Give the position of every Plasmodium parasite.
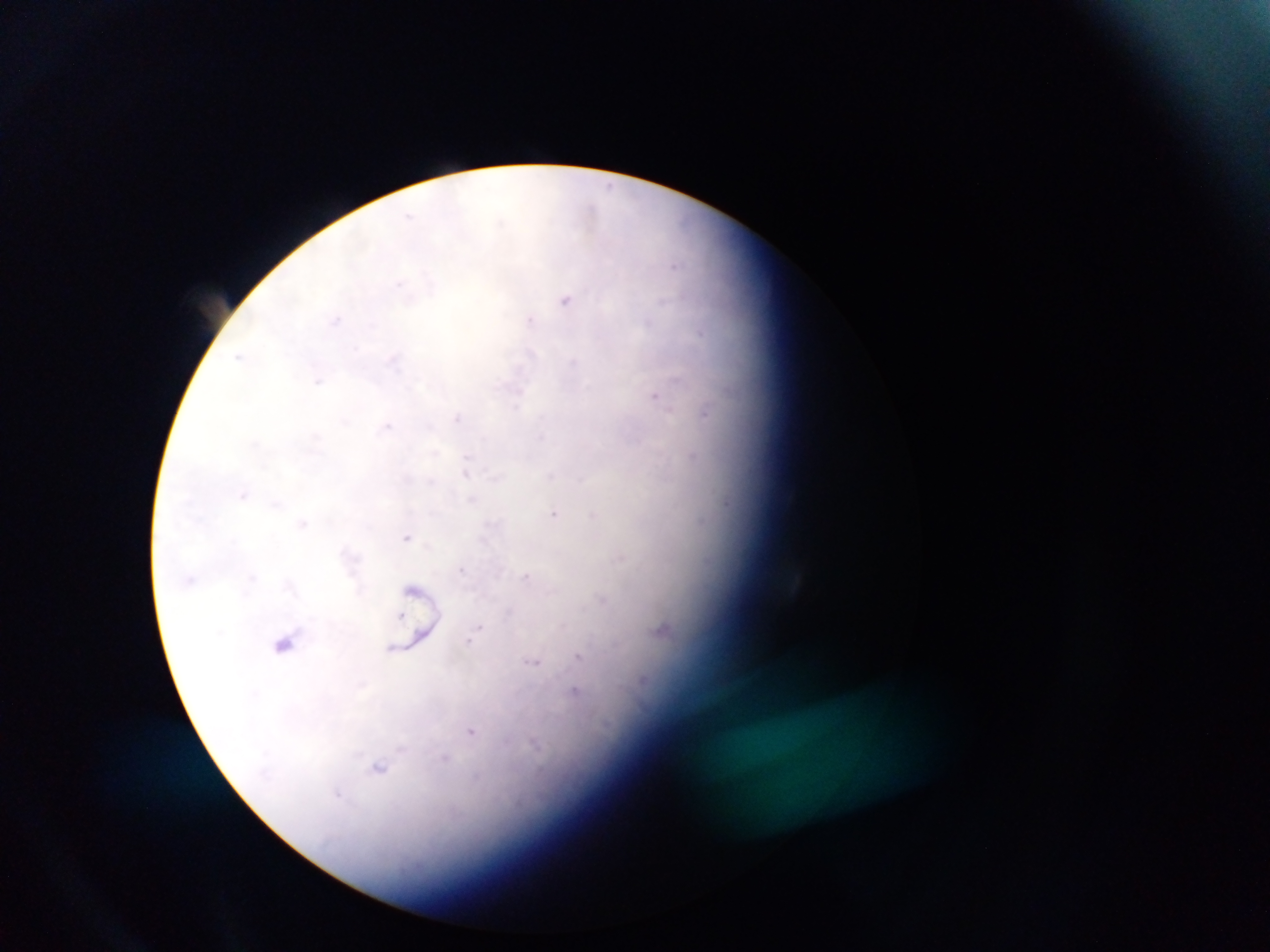
Approximate centers as {x, y} in pixels.
Plasmodium parasites: {592, 212}, {567, 299}, {530, 319}, {656, 395}, {705, 414}, {457, 417}, {388, 426}, {694, 455}, {466, 470}, {244, 494}, {726, 504}, {554, 513}, {594, 515}, {304, 523}, {407, 536}, {622, 558}, {463, 570}, {528, 576}, {602, 599}, {402, 616}, {479, 628}, {661, 630}, {471, 640}, {284, 644}, {579, 656}, {535, 662}, {577, 693}, {472, 731}, {379, 766}, {339, 794}.

Single field of view. Photographed through a microscope with a mobile-phone camera. Image is 1270×952 pixels. Collected in Ghana. Thick blood smear.